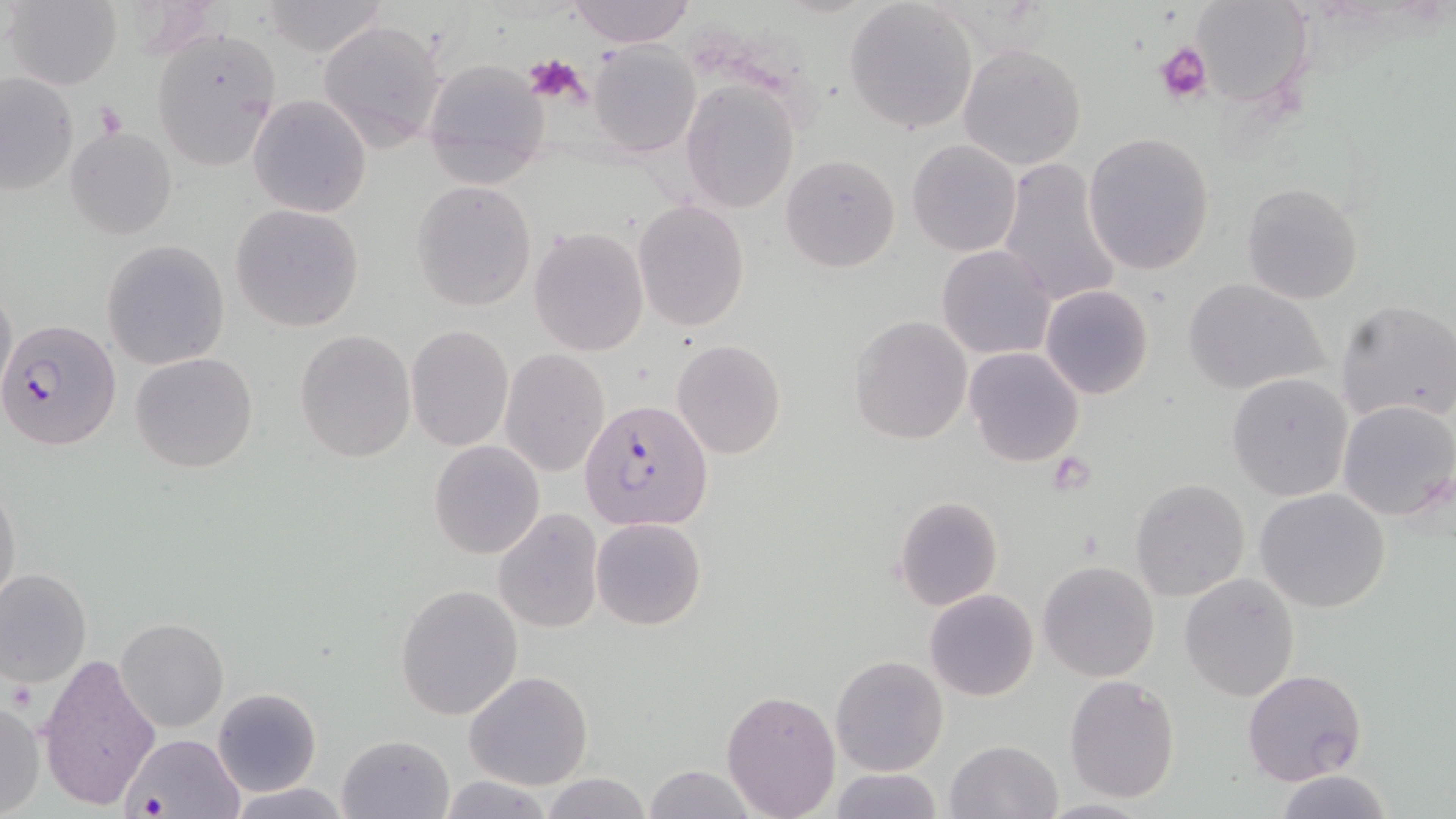 Approximate bounding boxes as named x1/y1/x2/y2 corners in pixels. Platelet locations: (x1=1155, y1=41, x2=1211, y2=103), (x1=524, y1=53, x2=590, y2=108), (x1=95, y1=100, x2=126, y2=140), (x1=1047, y1=451, x2=1096, y2=495), (x1=8, y1=678, x2=38, y2=713). Plasmodium falciparum-infected red blood cell locations: (x1=1, y1=317, x2=121, y2=451), (x1=578, y1=397, x2=713, y2=531), (x1=121, y1=735, x2=244, y2=819). Uninfected red blood cell locations: (x1=4, y1=0, x2=123, y2=90), (x1=566, y1=0, x2=696, y2=47), (x1=1190, y1=0, x2=1313, y2=106), (x1=844, y1=1, x2=980, y2=134), (x1=259, y1=2, x2=388, y2=57), (x1=318, y1=18, x2=448, y2=154), (x1=151, y1=26, x2=282, y2=172), (x1=589, y1=41, x2=700, y2=157), (x1=957, y1=42, x2=1087, y2=171), (x1=422, y1=58, x2=551, y2=189), (x1=2, y1=71, x2=77, y2=195), (x1=681, y1=80, x2=799, y2=214), (x1=249, y1=94, x2=372, y2=217), (x1=66, y1=127, x2=177, y2=239), (x1=1084, y1=131, x2=1216, y2=275), (x1=906, y1=139, x2=1023, y2=256), (x1=781, y1=153, x2=901, y2=273), (x1=994, y1=159, x2=1124, y2=310), (x1=411, y1=181, x2=537, y2=311), (x1=1241, y1=181, x2=1364, y2=303), (x1=633, y1=200, x2=750, y2=332), (x1=231, y1=204, x2=365, y2=332), (x1=529, y1=227, x2=650, y2=356), (x1=102, y1=239, x2=229, y2=370), (x1=937, y1=245, x2=1056, y2=360), (x1=1183, y1=277, x2=1328, y2=396), (x1=0, y1=284, x2=17, y2=398), (x1=1041, y1=284, x2=1153, y2=400), (x1=1336, y1=299, x2=1456, y2=426), (x1=849, y1=314, x2=972, y2=445), (x1=406, y1=326, x2=513, y2=450), (x1=295, y1=330, x2=417, y2=462), (x1=671, y1=339, x2=787, y2=460), (x1=964, y1=347, x2=1085, y2=466), (x1=499, y1=349, x2=612, y2=478), (x1=130, y1=352, x2=258, y2=474), (x1=1226, y1=373, x2=1353, y2=501), (x1=1337, y1=398, x2=1455, y2=520), (x1=428, y1=440, x2=545, y2=559), (x1=0, y1=478, x2=22, y2=614), (x1=1131, y1=479, x2=1251, y2=601), (x1=1255, y1=487, x2=1391, y2=613), (x1=893, y1=495, x2=1004, y2=611), (x1=492, y1=509, x2=604, y2=633), (x1=591, y1=517, x2=707, y2=630), (x1=1038, y1=561, x2=1159, y2=681), (x1=0, y1=568, x2=92, y2=686), (x1=1180, y1=572, x2=1299, y2=700), (x1=396, y1=584, x2=523, y2=721), (x1=924, y1=589, x2=1039, y2=702), (x1=117, y1=618, x2=228, y2=732), (x1=38, y1=650, x2=164, y2=812), (x1=830, y1=654, x2=948, y2=776), (x1=1243, y1=669, x2=1367, y2=787), (x1=465, y1=672, x2=592, y2=790), (x1=1064, y1=674, x2=1181, y2=805), (x1=213, y1=688, x2=321, y2=797), (x1=722, y1=690, x2=841, y2=818), (x1=0, y1=699, x2=44, y2=818), (x1=337, y1=735, x2=454, y2=819), (x1=945, y1=739, x2=1062, y2=819), (x1=642, y1=765, x2=756, y2=819), (x1=826, y1=766, x2=947, y2=819), (x1=1276, y1=771, x2=1391, y2=818), (x1=540, y1=772, x2=654, y2=819), (x1=439, y1=776, x2=556, y2=817), (x1=223, y1=781, x2=356, y2=818). Slide-level diagnosis: Plasmodium falciparum. May-Grünwald-Giemsa-stained preparation. One field of a larger specimen. Captured at 1000x magnification. Optical microscopy. Thin blood smear. Image is 1456×819 pixels.